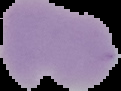

malaria status = uninfected
preparation = thin blood film
image size = 121×91 pixels
image type = segmented cell region with the area outside set to black